Point out leukocytes.
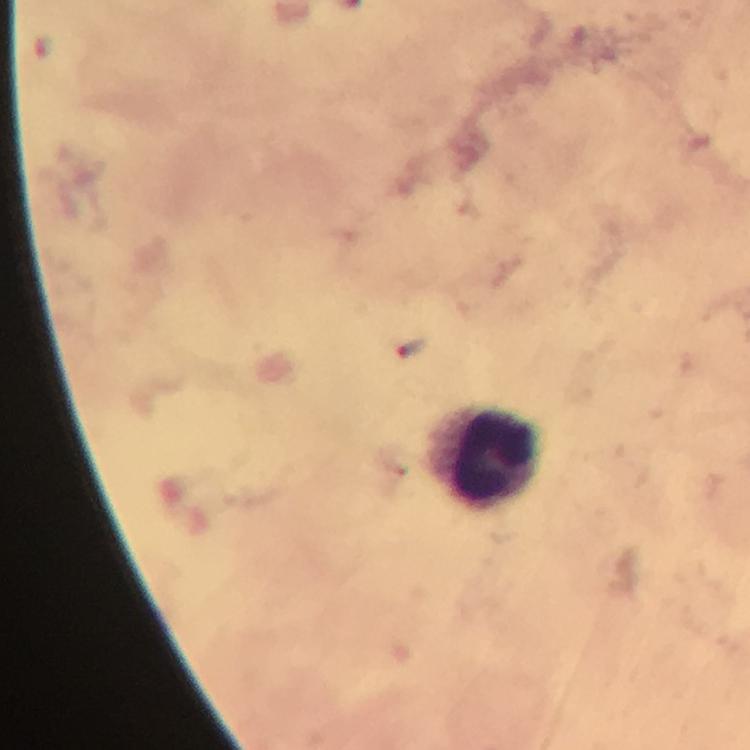

Approximate centers as (x, y) in pixels.
Leukocytes: (482, 462).

{
  "capture": "smartphone mounted on the microscope",
  "preparation": "thick blood film",
  "malaria_parasite_locations": "approximate centers as (x, y) in pixels: (408, 349)",
  "magnification": "100x",
  "context": "from a diagnostic examination for malaria",
  "immersion_oil": "used",
  "stain": "Giemsa",
  "cropped_from": "one field of view",
  "image_size": "750×750 pixels"
}